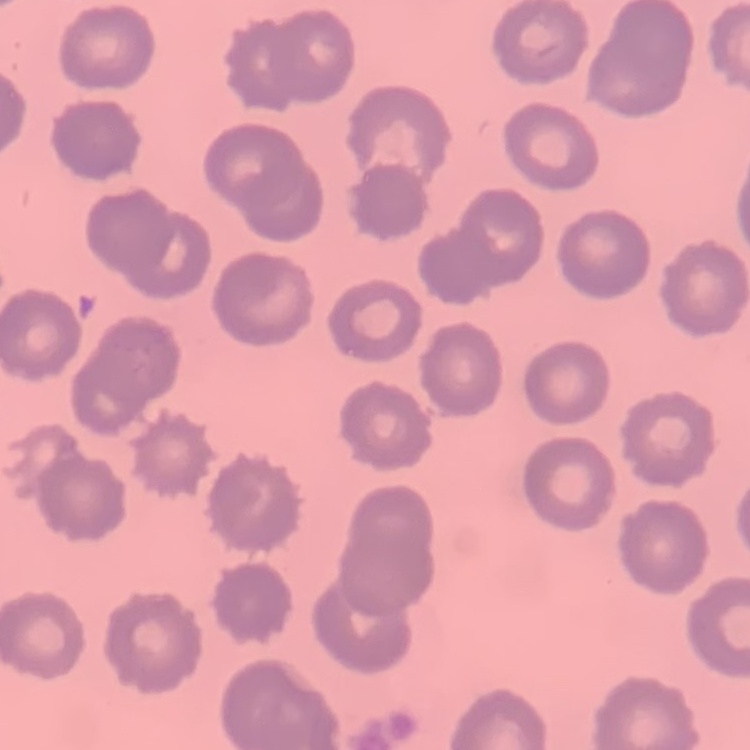

erythrocyte morphology = no rouleaux formation
preparation = thin blood film
image type = one tile cut from a larger photomicrograph
stain = Field's or Giemsa